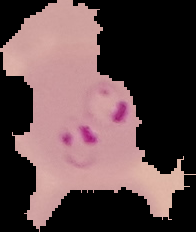

Segmented cell region on a black background. Malaria status: parasitized. From a thin blood film. Image is 196×232 pixels.